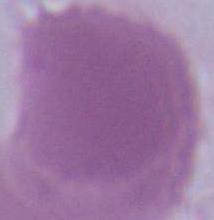
Summary:
  - Identification: red blood cell
  - Magnification: 1000x
  - Modality: photomicrograph